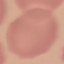
Summary:
  - Result: no malaria parasites seen
  - Capture: smartphone through the microscope eyepiece
  - Image type: cell patch, automatically extracted from a larger field of view and resized to 64 × 64 pixels
  - Stain: Giemsa
  - Preparation: thin smear